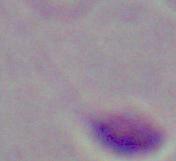

magnification: 1000x
modality: micrograph
identification: Leishmania